Describe the morphology of the erythrocytes.
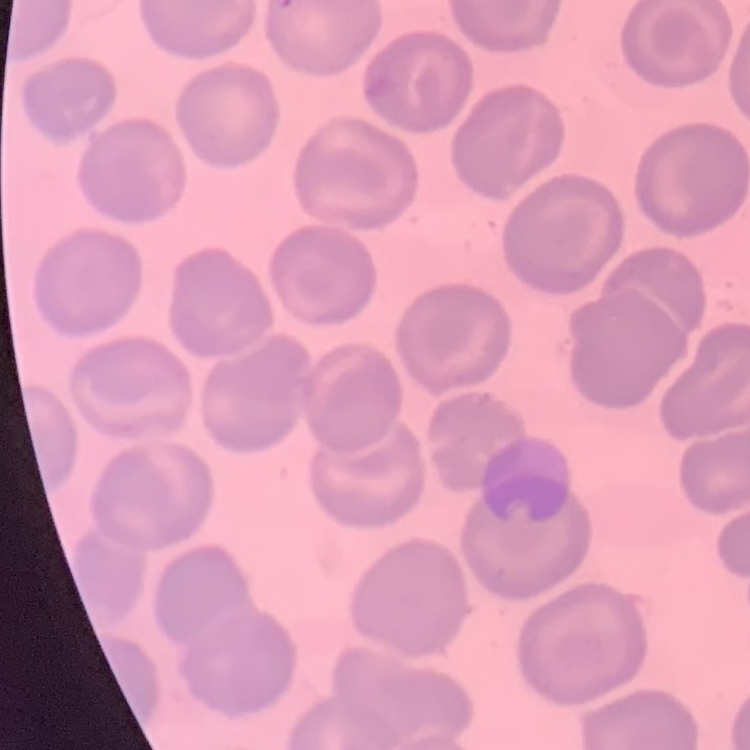

No rouleaux formation.

Summary:
  - Image type: square crop of a larger photomicrograph
  - Preparation: thin peripheral smear
  - Stain: Field's or Giemsa